Outline each Plasmodium ovale-infected red blood cell.
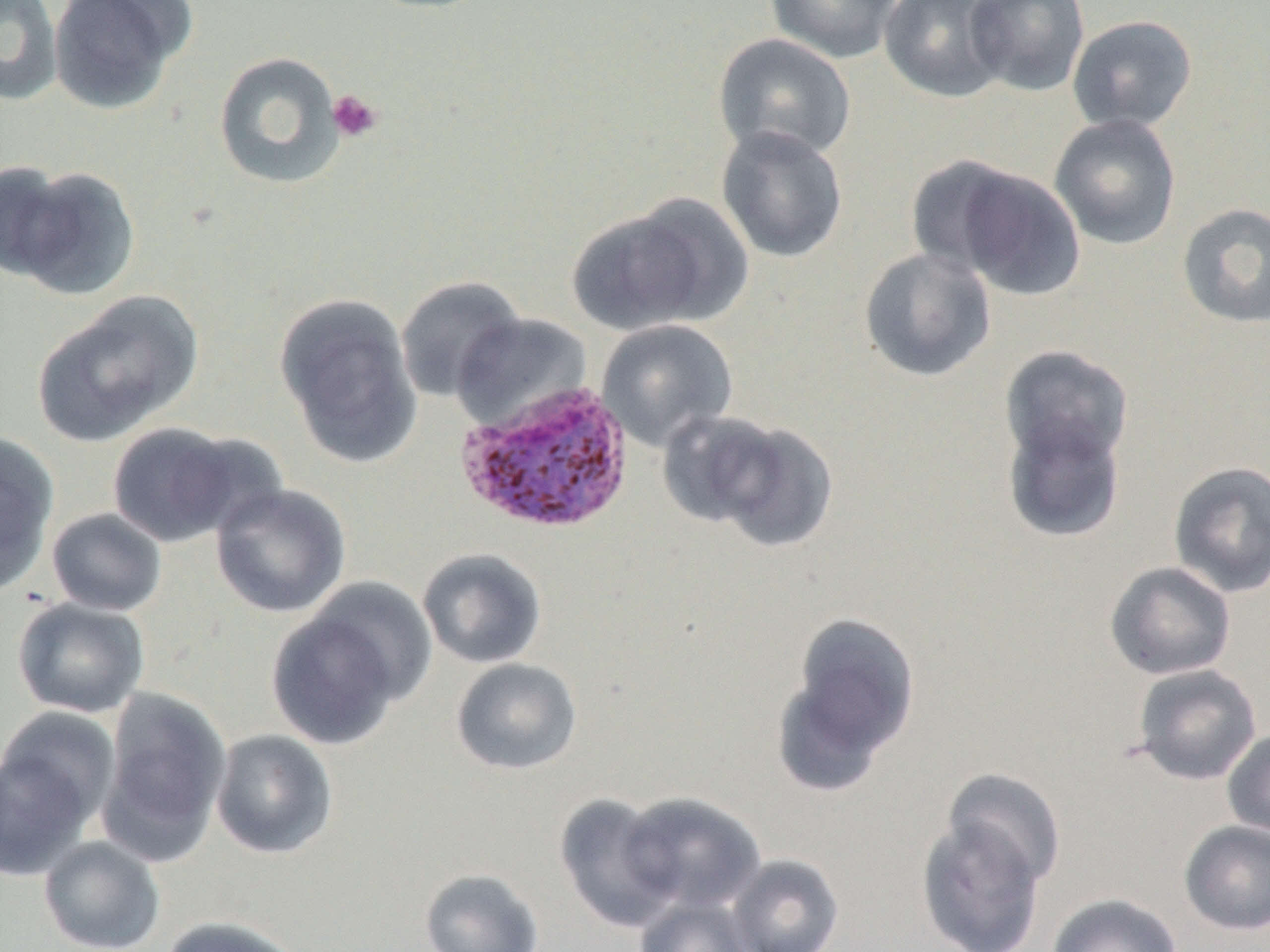
Approximate bounding boxes as named x1/y1/x2/y2 corners in pixels.
Plasmodium ovale-infected red blood cells: (x1=455, y1=378, x2=635, y2=536).

slide-level diagnosis = Plasmodium ovale
image size = 1270×952 pixels
platelet locations = approximate bounding boxes as named x1/y1/x2/y2 corners in pixels: (x1=327, y1=90, x2=384, y2=143)
uninfected red blood cell locations = approximate bounding boxes as named x1/y1/x2/y2 corners in pixels: (x1=0, y1=0, x2=63, y2=106), (x1=47, y1=0, x2=192, y2=115), (x1=765, y1=0, x2=903, y2=64), (x1=878, y1=0, x2=1011, y2=102), (x1=964, y1=0, x2=1091, y2=97), (x1=1066, y1=15, x2=1198, y2=134), (x1=712, y1=33, x2=857, y2=162), (x1=213, y1=51, x2=346, y2=190), (x1=1048, y1=114, x2=1182, y2=250), (x1=716, y1=125, x2=849, y2=263), (x1=905, y1=154, x2=1030, y2=276), (x1=0, y1=160, x2=76, y2=281), (x1=946, y1=163, x2=1086, y2=301), (x1=6, y1=165, x2=141, y2=300), (x1=564, y1=203, x2=723, y2=335), (x1=1177, y1=203, x2=1270, y2=329), (x1=859, y1=247, x2=996, y2=382), (x1=395, y1=276, x2=526, y2=403), (x1=33, y1=293, x2=202, y2=446), (x1=274, y1=293, x2=424, y2=467), (x1=451, y1=313, x2=591, y2=431), (x1=596, y1=320, x2=738, y2=452), (x1=999, y1=345, x2=1133, y2=472), (x1=1001, y1=410, x2=1127, y2=543), (x1=675, y1=412, x2=838, y2=551), (x1=107, y1=422, x2=255, y2=547), (x1=0, y1=431, x2=59, y2=596), (x1=1168, y1=460, x2=1270, y2=598), (x1=210, y1=483, x2=352, y2=618), (x1=46, y1=507, x2=168, y2=617), (x1=417, y1=547, x2=547, y2=668), (x1=1104, y1=561, x2=1236, y2=680), (x1=304, y1=575, x2=439, y2=712), (x1=12, y1=597, x2=150, y2=719), (x1=265, y1=598, x2=413, y2=751), (x1=785, y1=612, x2=920, y2=774), (x1=450, y1=657, x2=583, y2=775), (x1=1131, y1=664, x2=1262, y2=785), (x1=99, y1=685, x2=232, y2=864), (x1=0, y1=704, x2=122, y2=828), (x1=1222, y1=728, x2=1270, y2=839), (x1=210, y1=729, x2=339, y2=859), (x1=1, y1=747, x2=95, y2=882), (x1=942, y1=768, x2=1067, y2=888), (x1=617, y1=791, x2=766, y2=915), (x1=554, y1=792, x2=682, y2=932), (x1=916, y1=816, x2=1047, y2=952), (x1=1179, y1=820, x2=1270, y2=935), (x1=38, y1=835, x2=165, y2=952), (x1=727, y1=853, x2=844, y2=952), (x1=419, y1=868, x2=544, y2=952), (x1=1046, y1=892, x2=1182, y2=952), (x1=634, y1=895, x2=758, y2=952), (x1=158, y1=915, x2=306, y2=952)
preparation = thin blood film
modality = light microscopy
magnification = 1000x
field of view = one of a larger specimen